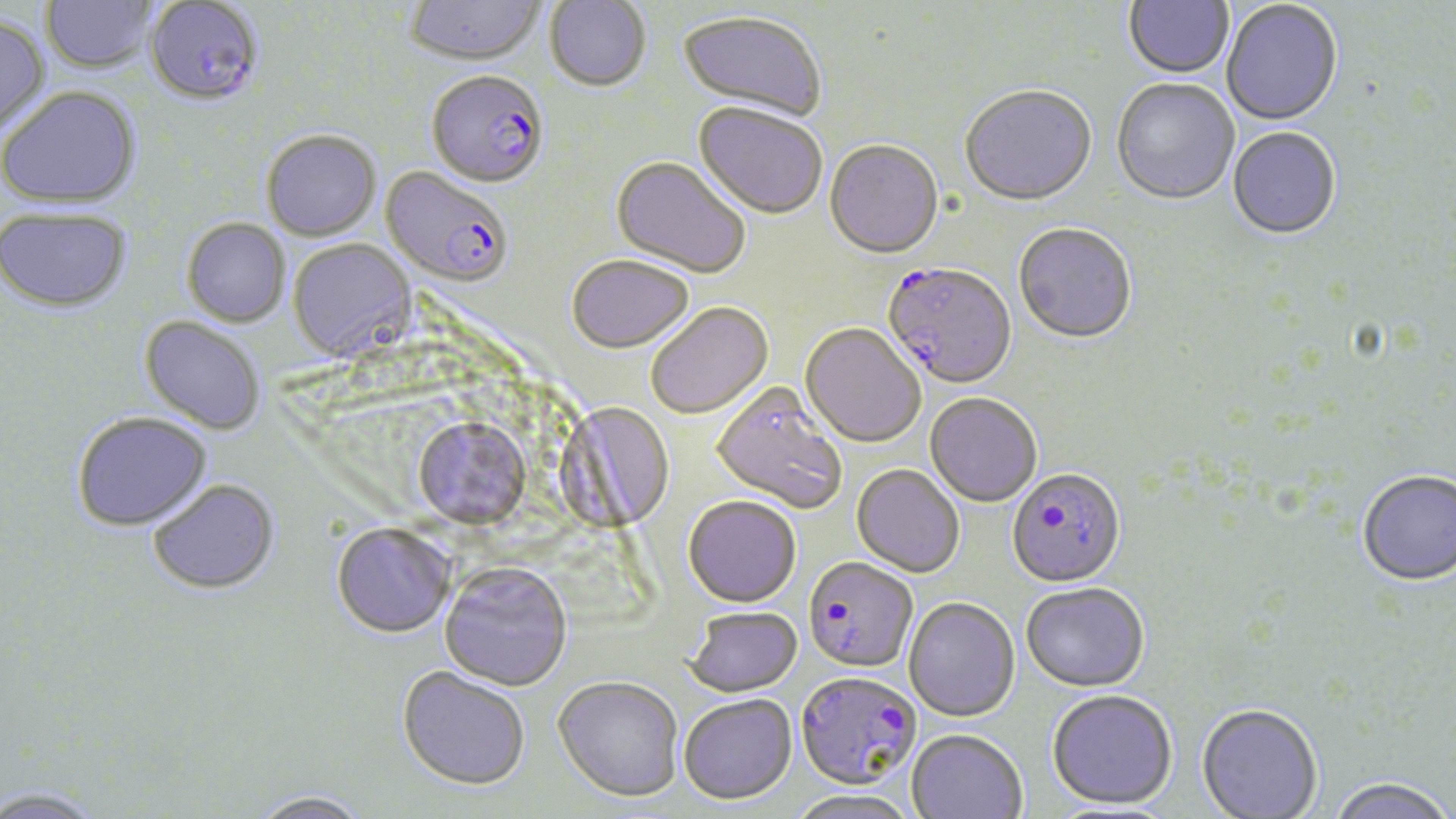
slide-level diagnosis = Plasmodium falciparum
preparation = thin blood smear
Plasmodium falciparum-infected red blood cell locations = approximate bounding boxes as (x1, y1, x2, y2) in pixels: (144, 2, 264, 111), (426, 73, 549, 191), (380, 168, 513, 291), (881, 264, 1016, 390), (1007, 468, 1126, 588), (803, 556, 918, 673), (796, 670, 922, 789)
stain = May-Grünwald-Giemsa
field of view = one of a larger specimen
uninfected red blood cell locations = approximate bounding boxes as (x1, y1, x2, y2) in pixels: (42, 0, 159, 75), (1123, 0, 1235, 81), (404, 1, 546, 69), (544, 1, 651, 93), (1221, 1, 1343, 128), (675, 12, 826, 124), (0, 16, 49, 139), (1111, 80, 1239, 207), (1, 88, 141, 211), (960, 88, 1097, 209), (692, 104, 828, 223), (1228, 129, 1341, 241), (261, 132, 382, 243), (824, 142, 944, 262), (610, 157, 750, 280), (1, 210, 132, 316), (182, 220, 291, 328), (1013, 225, 1137, 346), (288, 240, 416, 362), (567, 255, 694, 354), (645, 302, 773, 419), (138, 318, 264, 436), (800, 324, 925, 448), (710, 384, 848, 517), (924, 393, 1043, 508), (558, 403, 681, 536), (410, 410, 532, 530), (72, 415, 213, 534), (851, 464, 965, 578), (1358, 471, 1456, 588), (148, 481, 280, 598), (683, 495, 801, 607), (332, 526, 456, 639), (439, 565, 572, 692), (1021, 582, 1150, 692), (903, 597, 1020, 722), (684, 606, 802, 697), (397, 667, 530, 790), (553, 674, 685, 801), (1046, 688, 1178, 810), (678, 693, 797, 804), (1196, 706, 1323, 819), (907, 728, 1027, 818), (1326, 779, 1455, 819), (2, 787, 108, 819), (788, 789, 920, 819), (245, 790, 375, 819)
image size = 1456×819 pixels
modality = optical microscopy
magnification = 1000x